State the blood parasite species.
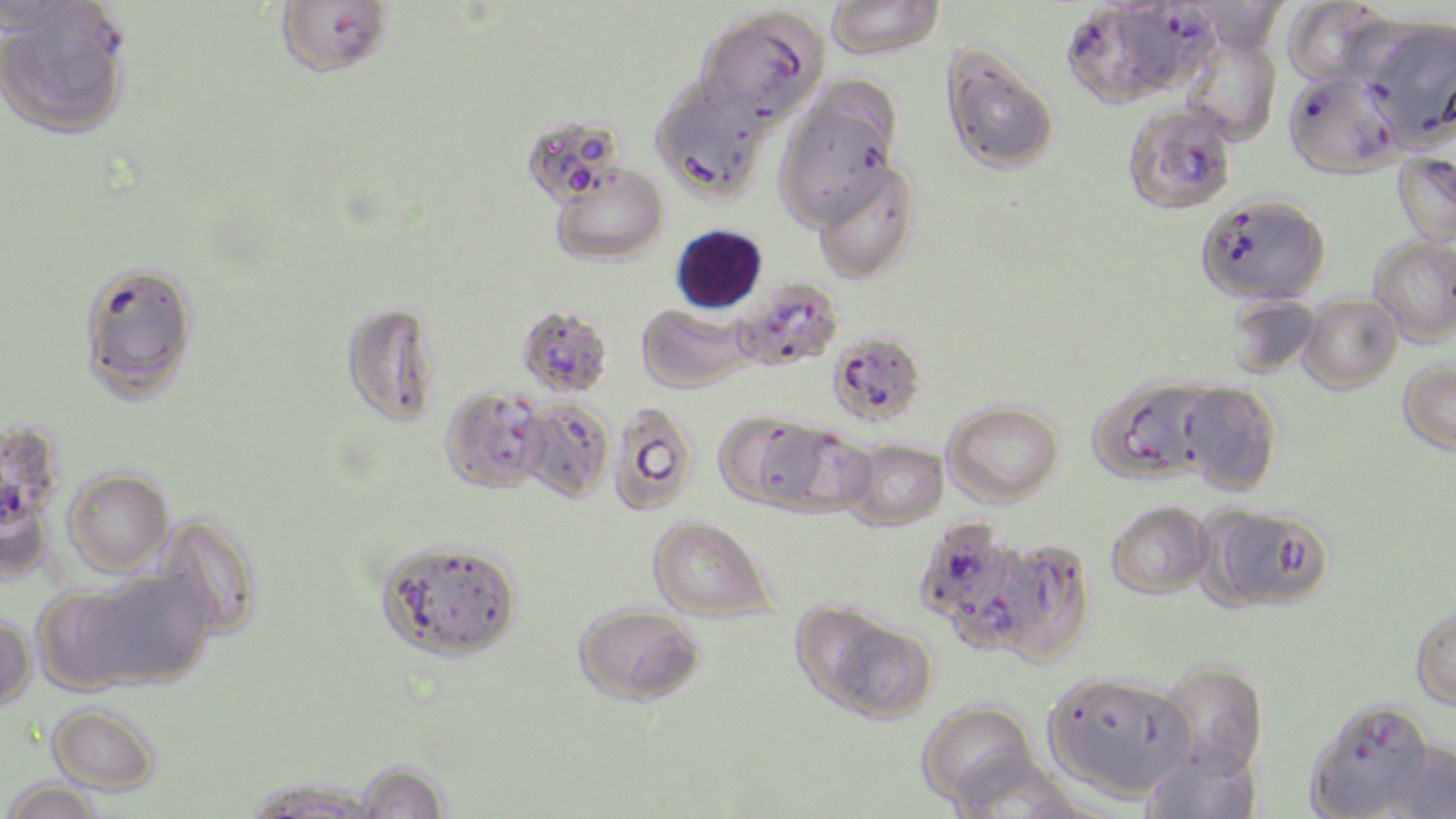
Plasmodium falciparum.

Summary:
  - Coordinate format: approximate bounding boxes as named x1/y1/x2/y2 corners in pixels
  - Plasmodium falciparum-infected red blood cell locations: (x1=274, y1=0, x2=394, y2=79), (x1=1, y1=1, x2=135, y2=102), (x1=1113, y1=1, x2=1223, y2=92), (x1=1061, y1=3, x2=1181, y2=108), (x1=1284, y1=70, x2=1402, y2=177), (x1=1122, y1=103, x2=1238, y2=216), (x1=1196, y1=193, x2=1329, y2=305), (x1=732, y1=277, x2=844, y2=371), (x1=516, y1=304, x2=613, y2=398), (x1=831, y1=334, x2=925, y2=427), (x1=1, y1=421, x2=56, y2=531), (x1=914, y1=517, x2=1033, y2=648), (x1=982, y1=540, x2=1095, y2=664), (x1=1304, y1=698, x2=1436, y2=819)
  - Uninfected red blood cell locations: (x1=825, y1=0, x2=945, y2=60), (x1=1284, y1=0, x2=1398, y2=88), (x1=695, y1=7, x2=829, y2=131), (x1=1356, y1=18, x2=1455, y2=147), (x1=1180, y1=30, x2=1281, y2=147), (x1=941, y1=46, x2=1060, y2=175), (x1=650, y1=79, x2=769, y2=203), (x1=773, y1=88, x2=900, y2=230), (x1=521, y1=113, x2=627, y2=207), (x1=1393, y1=151, x2=1456, y2=245), (x1=811, y1=160, x2=918, y2=283), (x1=550, y1=165, x2=668, y2=266), (x1=1369, y1=237, x2=1455, y2=346), (x1=77, y1=259, x2=199, y2=401), (x1=1226, y1=295, x2=1321, y2=378), (x1=1299, y1=295, x2=1402, y2=393), (x1=341, y1=301, x2=440, y2=426), (x1=636, y1=303, x2=754, y2=393), (x1=1398, y1=360, x2=1456, y2=455), (x1=1090, y1=377, x2=1217, y2=483), (x1=1178, y1=382, x2=1283, y2=495), (x1=439, y1=386, x2=547, y2=494), (x1=515, y1=399, x2=614, y2=502), (x1=942, y1=400, x2=1063, y2=506), (x1=608, y1=402, x2=699, y2=516), (x1=714, y1=410, x2=827, y2=511), (x1=760, y1=423, x2=876, y2=517), (x1=843, y1=439, x2=948, y2=530), (x1=63, y1=468, x2=174, y2=575), (x1=1107, y1=501, x2=1212, y2=598), (x1=1202, y1=504, x2=1335, y2=612), (x1=154, y1=513, x2=264, y2=640), (x1=648, y1=515, x2=776, y2=621), (x1=376, y1=539, x2=523, y2=662), (x1=73, y1=570, x2=216, y2=689), (x1=573, y1=603, x2=705, y2=706), (x1=799, y1=604, x2=937, y2=723), (x1=1410, y1=604, x2=1456, y2=710), (x1=0, y1=614, x2=36, y2=711), (x1=1157, y1=661, x2=1268, y2=778), (x1=1043, y1=671, x2=1195, y2=801), (x1=916, y1=700, x2=1039, y2=810), (x1=47, y1=701, x2=161, y2=794), (x1=1385, y1=740, x2=1456, y2=819), (x1=1141, y1=742, x2=1264, y2=819), (x1=943, y1=751, x2=1083, y2=817), (x1=353, y1=760, x2=452, y2=818), (x1=243, y1=777, x2=380, y2=818), (x1=2, y1=779, x2=104, y2=819)
  - Field of view: single
  - Stain: May-Grünwald-Giemsa
  - Magnification: 1000x
  - Preparation: thin blood film
  - Image size: 1456×819 pixels
  - Modality: light microscopy